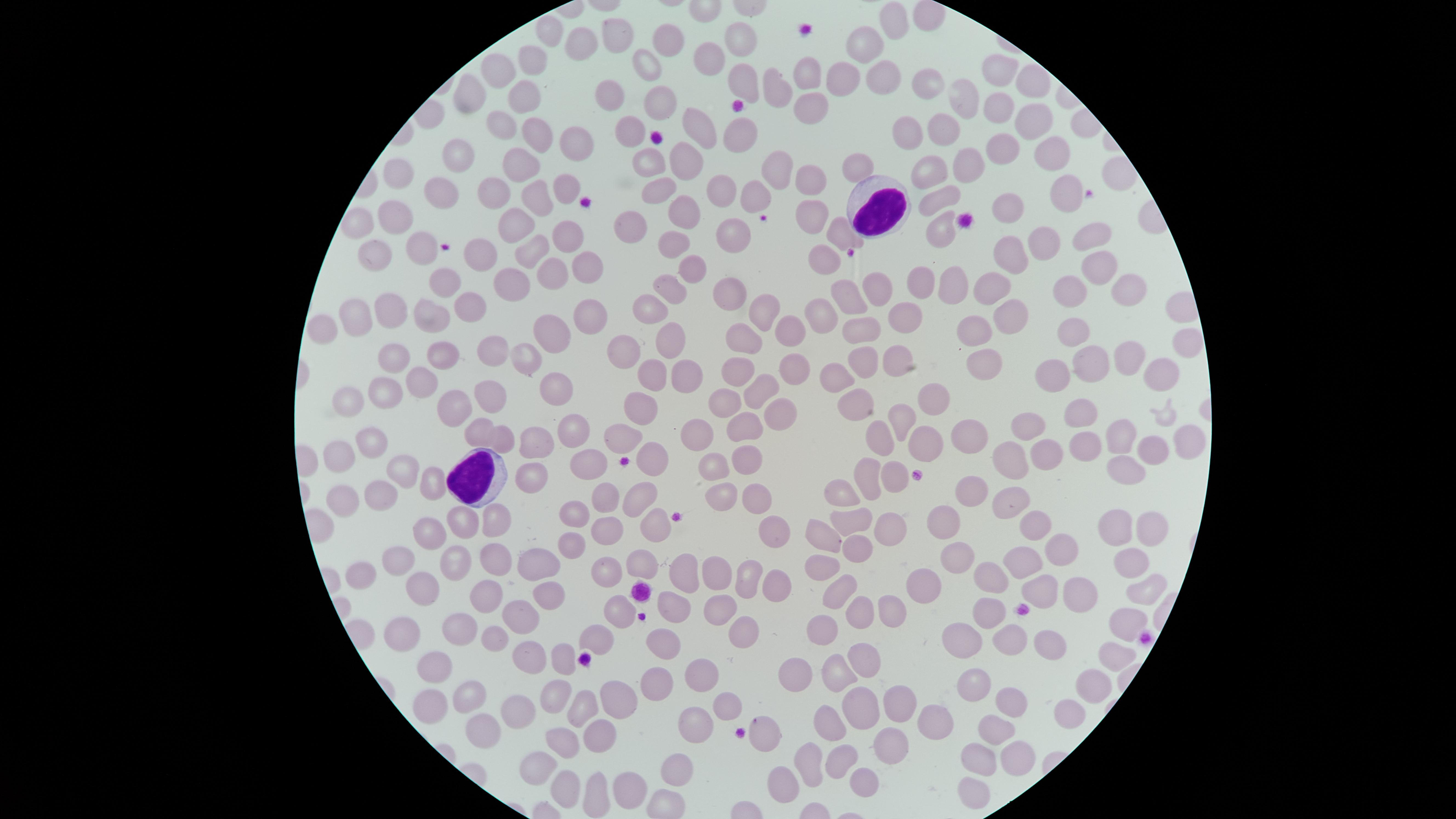
field_of_view: single
image_size: 1456×819 pixels
capture: smartphone photograph through the microscope eyepiece
white_blood_cells: 'approximate marker points as (x, y) in pixels: (878, 208), (475, 479)'
stain: Giemsa
presence: no malaria parasites detected
visible_region: circular
uninfected_red_blood_cells: 'approximate marker points as (x, y) in pixels: (891, 24), (549, 32), (613, 35), (739, 37), (662, 39), (579, 42), (865, 49), (534, 60), (709, 63), (497, 64), (646, 65), (993, 70), (881, 73), (807, 78), (841, 80), (743, 83), (780, 83), (925, 86), (1024, 86), (527, 90), (608, 91), (474, 94), (656, 97), (959, 100), (816, 104), (1009, 104), (1028, 118), (505, 121), (916, 122), (634, 123), (940, 128), (694, 130), (733, 131), (535, 133), (564, 144), (1052, 152), (457, 153), (1006, 153), (644, 154), (520, 158), (684, 162), (967, 165), (856, 168), (777, 170), (401, 172), (931, 174), (809, 180), (565, 185), (446, 186), (653, 186), (1054, 190), (492, 191), (717, 191), (749, 191), (536, 197), (943, 197), (997, 198), (809, 210), (398, 212), (676, 212), (513, 219), (637, 219), (362, 220), (730, 227), (837, 232), (943, 232), (1091, 233), (567, 238), (674, 239), (1044, 243), (377, 245), (417, 247), (537, 249), (480, 252), (1009, 253), (819, 259), (688, 264), (1091, 266), (580, 267), (543, 271), (923, 282), (951, 282), (442, 284), (515, 284), (993, 285), (1075, 285), (667, 286), (727, 288), (1128, 291), (877, 293), (468, 303), (849, 303), (651, 308), (386, 309), (591, 310), (1018, 310), (359, 312), (763, 312), (909, 316), (816, 317), (426, 318), (329, 325), (789, 330), (975, 331), (550, 334), (670, 335), (747, 337), (864, 337), (1066, 337), (1183, 342), (497, 349), (441, 353), (625, 353), (908, 357), (1121, 357), (864, 358), (527, 359), (393, 360), (990, 362), (1087, 363), (791, 366), (652, 370), (736, 370), (1160, 371), (684, 373), (1058, 373), (421, 376), (839, 379), (763, 387), (555, 388), (380, 389), (488, 393), (929, 395), (347, 400), (728, 400), (858, 400), (453, 401), (642, 405), (1076, 409), (775, 410), (900, 416), (1026, 424), (478, 427), (742, 427), (568, 428), (700, 432), (968, 433), (623, 434), (1122, 435), (1184, 436), (369, 439), (503, 439), (930, 439), (532, 440), (882, 440), (1088, 444), (1152, 445), (741, 451), (340, 452), (652, 455), (1050, 456), (1011, 457), (708, 460), (586, 462), (1124, 467), (400, 469), (869, 471), (528, 477), (893, 477), (426, 487), (967, 489), (1011, 489), (842, 494), (717, 495), (756, 495), (608, 500), (378, 501), (344, 502), (638, 502), (576, 514), (498, 518), (850, 520), (463, 521), (944, 521), (1033, 521), (880, 524), (430, 527), (1107, 527), (1145, 528), (654, 530), (770, 531), (607, 534), (823, 538), (856, 547), (571, 549), (1058, 549), (489, 560), (957, 560), (400, 561), (458, 561), (643, 561), (1130, 561), (534, 565), (1024, 565), (827, 566), (366, 568), (716, 570), (605, 573), (745, 575), (771, 576), (682, 578), (925, 581), (991, 581), (420, 585), (1038, 588), (1146, 588), (841, 591), (486, 592), (1080, 596), (547, 597), (888, 604), (717, 608), (524, 612), (627, 612), (675, 612), (859, 612), (991, 612), (1123, 621), (741, 624), (469, 628), (819, 629), (397, 632), (1006, 633), (961, 634), (493, 639), (589, 639), (661, 644), (1051, 645), (862, 655), (528, 656), (1110, 659), (555, 660), (446, 663), (802, 669), (702, 670), (838, 670), (662, 678), (978, 684), (1093, 688), (552, 690), (471, 694), (433, 698), (728, 698), (896, 702), (582, 706), (1011, 706), (614, 707), (1069, 709), (514, 714), (856, 714), (928, 714), (694, 722), (830, 725), (479, 729), (601, 729), (997, 730), (769, 738), (564, 741), (886, 742), (840, 756), (1014, 759), (809, 761), (978, 761), (676, 763), (534, 766), (858, 774), (559, 783), (628, 784), (777, 784), (595, 792), (969, 794)'
preparation: thin smear of blood